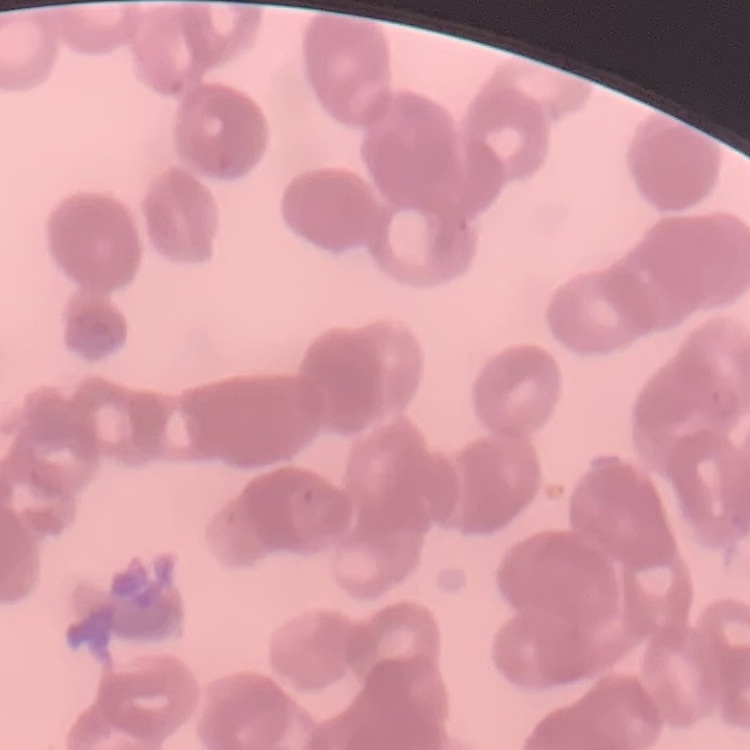

red blood cell morphology = rouleaux formation
preparation = thin peripheral smear
stain = Field's or Giemsa
image type = one tile cut from a larger photomicrograph